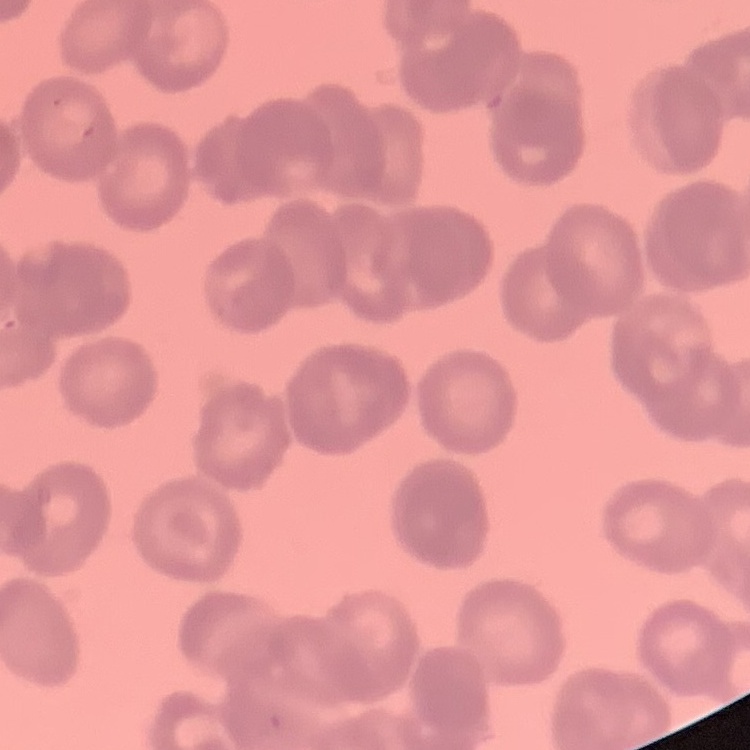

{
  "red_blood_cell_morphology": "rouleaux formation",
  "preparation": "thin peripheral smear",
  "image_type": "one tile cut from a larger photomicrograph",
  "stain": "Field's or Giemsa"
}